Give the position of every leukocyte visible.
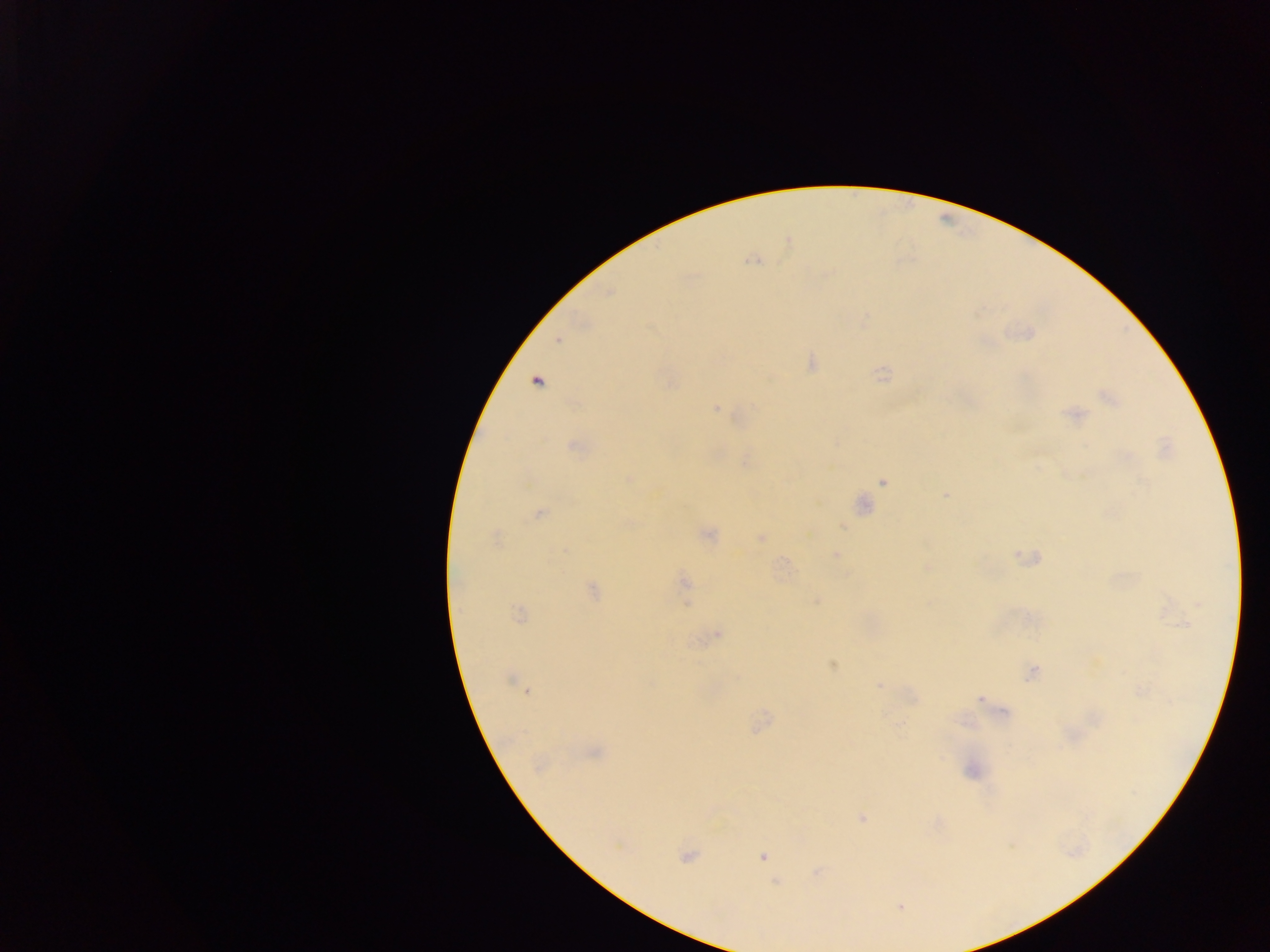

No leukocytes observed.

Approximate centers as {x, y} in pixels. Plasmodium parasite locations: {753, 260}, {557, 340}, {812, 364}, {884, 375}, {536, 381}, {1107, 396}, {717, 408}, {1076, 414}, {574, 447}, {629, 478}, {883, 482}, {946, 494}, {539, 514}, {842, 526}, {708, 534}, {495, 536}, {761, 538}, {836, 555}, {685, 582}, {592, 591}, {1199, 604}, {519, 614}, {1184, 624}, {717, 634}, {832, 665}, {1032, 673}, {510, 680}, {879, 686}, {526, 691}, {979, 699}, {595, 753}, {861, 818}, {686, 857}, {763, 857}, {776, 882}, {900, 907}. Thick blood film. Photographed through a microscope with a mobile-phone camera. Sample from Ghana. Image is 1270×952 pixels. Single field of view.